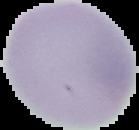

Summary:
  - Image size: 139×130 pixels
  - Image type: cell region segmented out of the field of view; surrounding area masked to black
  - Preparation: thin blood smear
  - Result: no Plasmodium parasites seen